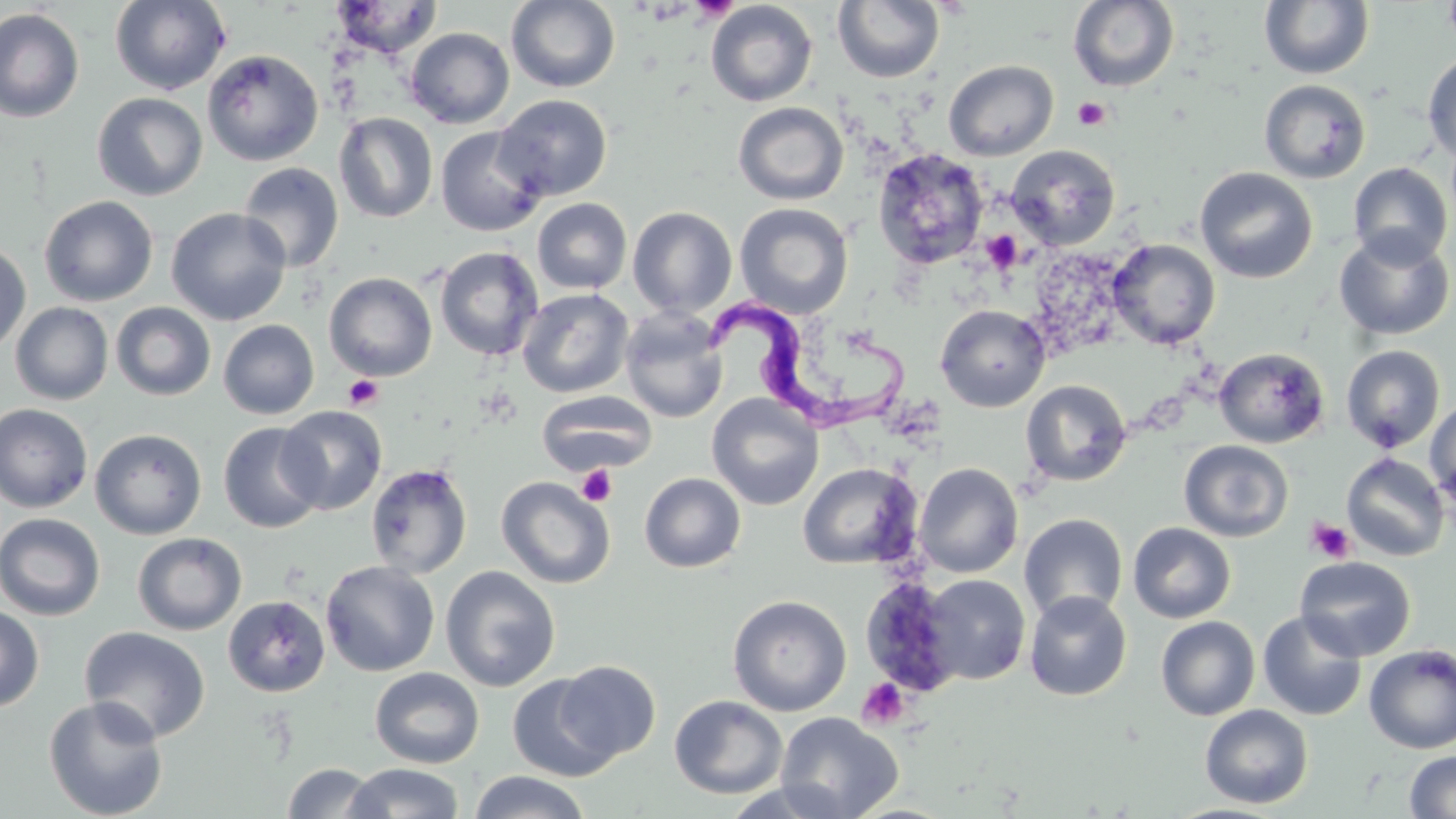

slide-level diagnosis = Trypanosoma brucei
image size = 1456×819 pixels
stain = May-Grünwald-Giemsa
modality = optical microscopy
Trypanosoma brucei locations = approximate bounding boxes as named x1/y1/x2/y2 corners in pixels: (x1=705, y1=294, x2=912, y2=431)
platelet locations = approximate bounding boxes as named x1/y1/x2/y2 corners in pixels: (x1=689, y1=0, x2=739, y2=23), (x1=1072, y1=97, x2=1111, y2=130), (x1=981, y1=230, x2=1023, y2=273), (x1=343, y1=374, x2=384, y2=409), (x1=576, y1=464, x2=618, y2=507), (x1=1306, y1=517, x2=1356, y2=563), (x1=857, y1=678, x2=909, y2=729)
field of view = single
magnification = 1000x
uninfected red blood cell locations = approximate bounding boxes as named x1/y1/x2/y2 corners in pixels: (x1=109, y1=0, x2=232, y2=95), (x1=505, y1=0, x2=621, y2=94), (x1=831, y1=0, x2=945, y2=84), (x1=103, y1=1, x2=222, y2=199), (x1=329, y1=1, x2=444, y2=59), (x1=705, y1=1, x2=818, y2=107), (x1=1068, y1=1, x2=1180, y2=92), (x1=1259, y1=1, x2=1374, y2=80), (x1=1441, y1=1, x2=1456, y2=53), (x1=0, y1=8, x2=85, y2=124), (x1=405, y1=27, x2=514, y2=129), (x1=202, y1=49, x2=324, y2=166), (x1=1422, y1=50, x2=1456, y2=165), (x1=943, y1=60, x2=1059, y2=161), (x1=1258, y1=79, x2=1371, y2=184), (x1=92, y1=92, x2=208, y2=200), (x1=493, y1=94, x2=613, y2=201), (x1=733, y1=101, x2=849, y2=205), (x1=334, y1=112, x2=438, y2=223), (x1=435, y1=126, x2=548, y2=236), (x1=1006, y1=144, x2=1120, y2=250), (x1=872, y1=149, x2=990, y2=271), (x1=238, y1=162, x2=344, y2=272), (x1=1347, y1=162, x2=1453, y2=268), (x1=1194, y1=166, x2=1318, y2=284), (x1=39, y1=195, x2=158, y2=306), (x1=531, y1=198, x2=632, y2=294), (x1=734, y1=203, x2=854, y2=319), (x1=628, y1=206, x2=738, y2=317), (x1=166, y1=207, x2=291, y2=325), (x1=1333, y1=229, x2=1454, y2=341), (x1=1107, y1=238, x2=1221, y2=350), (x1=0, y1=241, x2=31, y2=355), (x1=434, y1=246, x2=544, y2=361), (x1=323, y1=272, x2=437, y2=381), (x1=517, y1=288, x2=634, y2=398), (x1=10, y1=302, x2=113, y2=405), (x1=111, y1=302, x2=216, y2=401), (x1=934, y1=304, x2=1051, y2=412), (x1=620, y1=307, x2=729, y2=423), (x1=218, y1=319, x2=319, y2=419), (x1=1341, y1=345, x2=1445, y2=453), (x1=1213, y1=347, x2=1329, y2=448), (x1=1021, y1=379, x2=1132, y2=487), (x1=537, y1=391, x2=657, y2=475), (x1=707, y1=394, x2=823, y2=510), (x1=1426, y1=398, x2=1456, y2=505), (x1=1, y1=403, x2=93, y2=513), (x1=276, y1=406, x2=387, y2=515), (x1=218, y1=422, x2=326, y2=533), (x1=90, y1=428, x2=207, y2=540), (x1=1179, y1=439, x2=1293, y2=542), (x1=1341, y1=453, x2=1450, y2=561), (x1=797, y1=462, x2=922, y2=570), (x1=914, y1=462, x2=1023, y2=578), (x1=366, y1=463, x2=473, y2=579), (x1=639, y1=472, x2=745, y2=572), (x1=496, y1=476, x2=616, y2=589), (x1=0, y1=513, x2=106, y2=621), (x1=1019, y1=513, x2=1128, y2=623), (x1=1127, y1=522, x2=1236, y2=623), (x1=131, y1=532, x2=247, y2=635), (x1=1294, y1=556, x2=1417, y2=661), (x1=320, y1=560, x2=439, y2=677), (x1=441, y1=565, x2=560, y2=691), (x1=921, y1=574, x2=1030, y2=685), (x1=864, y1=577, x2=981, y2=696), (x1=1024, y1=591, x2=1132, y2=701), (x1=728, y1=594, x2=852, y2=717), (x1=223, y1=595, x2=330, y2=697), (x1=0, y1=604, x2=44, y2=712), (x1=1257, y1=610, x2=1367, y2=721), (x1=1156, y1=616, x2=1260, y2=721), (x1=79, y1=626, x2=211, y2=744), (x1=1364, y1=644, x2=1456, y2=753), (x1=554, y1=660, x2=661, y2=762), (x1=370, y1=668, x2=484, y2=768), (x1=507, y1=673, x2=621, y2=782), (x1=43, y1=695, x2=169, y2=819), (x1=669, y1=695, x2=788, y2=799), (x1=1199, y1=704, x2=1313, y2=809), (x1=775, y1=712, x2=903, y2=819), (x1=1403, y1=750, x2=1456, y2=818), (x1=282, y1=763, x2=382, y2=818), (x1=344, y1=763, x2=466, y2=819), (x1=469, y1=770, x2=590, y2=819), (x1=719, y1=780, x2=856, y2=819)
preparation = thin blood film